Assess for Plasmodium parasites.
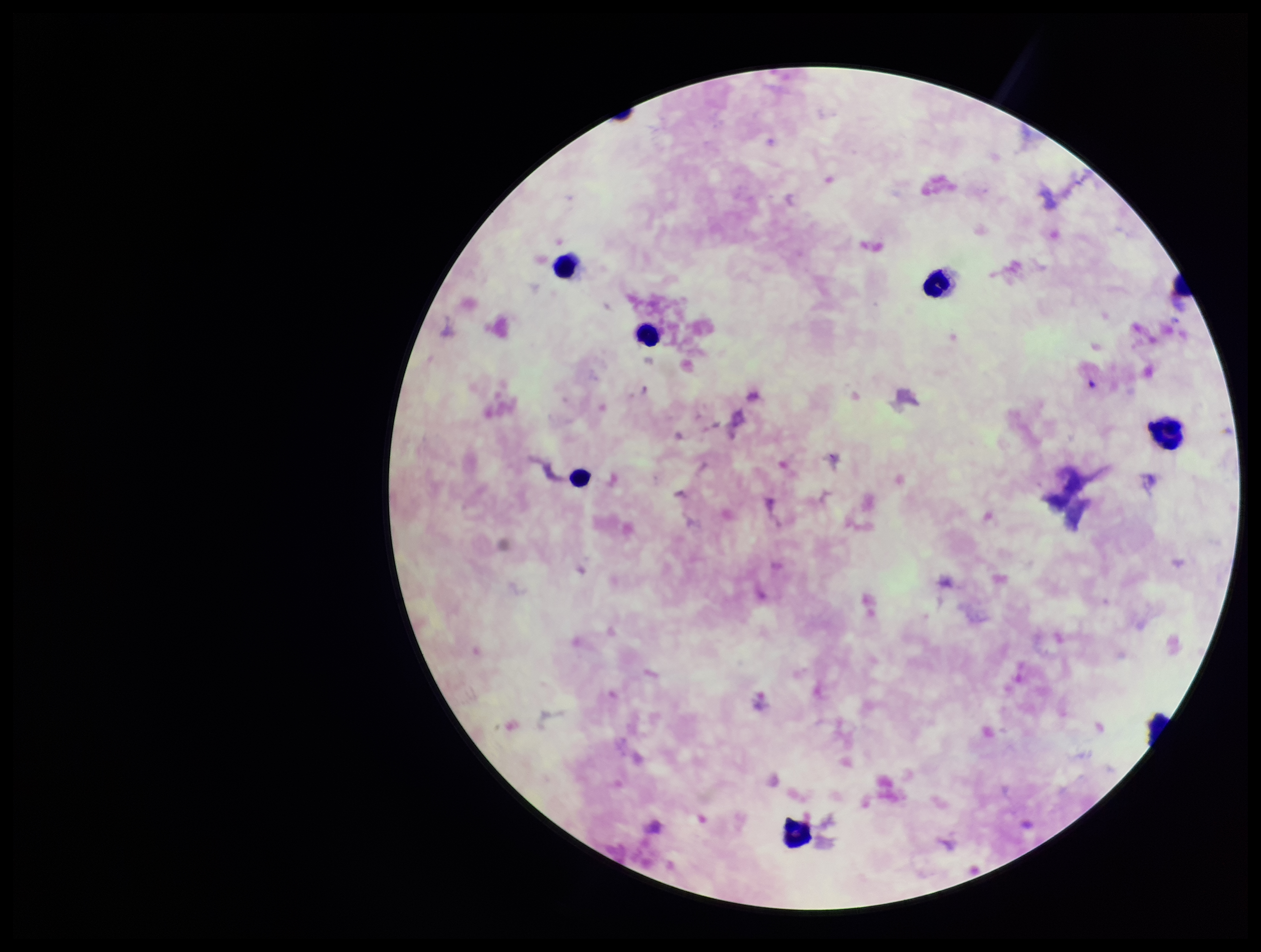
None seen.

image_size: 1261×952 pixels
leukocyte_count: 6
patient_malaria_status: positive
parasite_count: 0
species_reported_for_this_patient: Plasmodium falciparum
preparation: thick
field_of_view: single
capture: smartphone photograph through the microscope eyepiece
stain: Giemsa